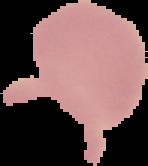

From a thin blood smear. Cell region segmented out of the field of view; the surrounding area is masked to black. Image is 148×166 pixels. Result: no malaria parasites detected.